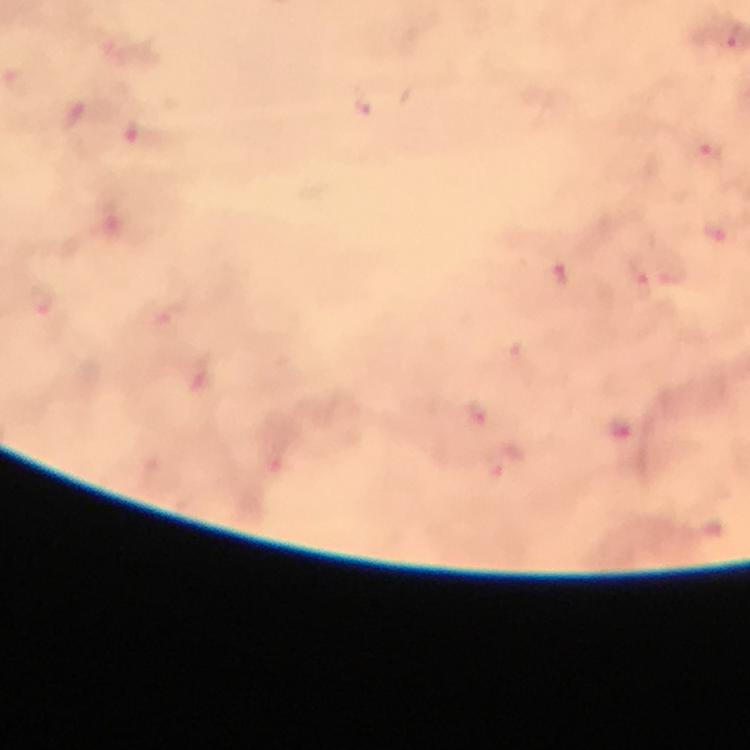

magnification = 100x
image size = 750×750 pixels
cropped from = a single field of view
preparation = thick smear
immersion oil = applied
stain = Giemsa
capture = smartphone camera through the microscope
malaria parasite locations = approximate object centers, in pixels from the top-left corner: (x=708, y=157), (x=716, y=234), (x=562, y=274)
context = from a diagnostic examination for malaria